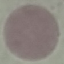 Malaria status: uninfected. Acquired by smartphone through the microscope eyepiece. Thin blood film. Cell patch, automatically extracted from a larger field of view and resized to 64 × 64 pixels. Giemsa-stained preparation.